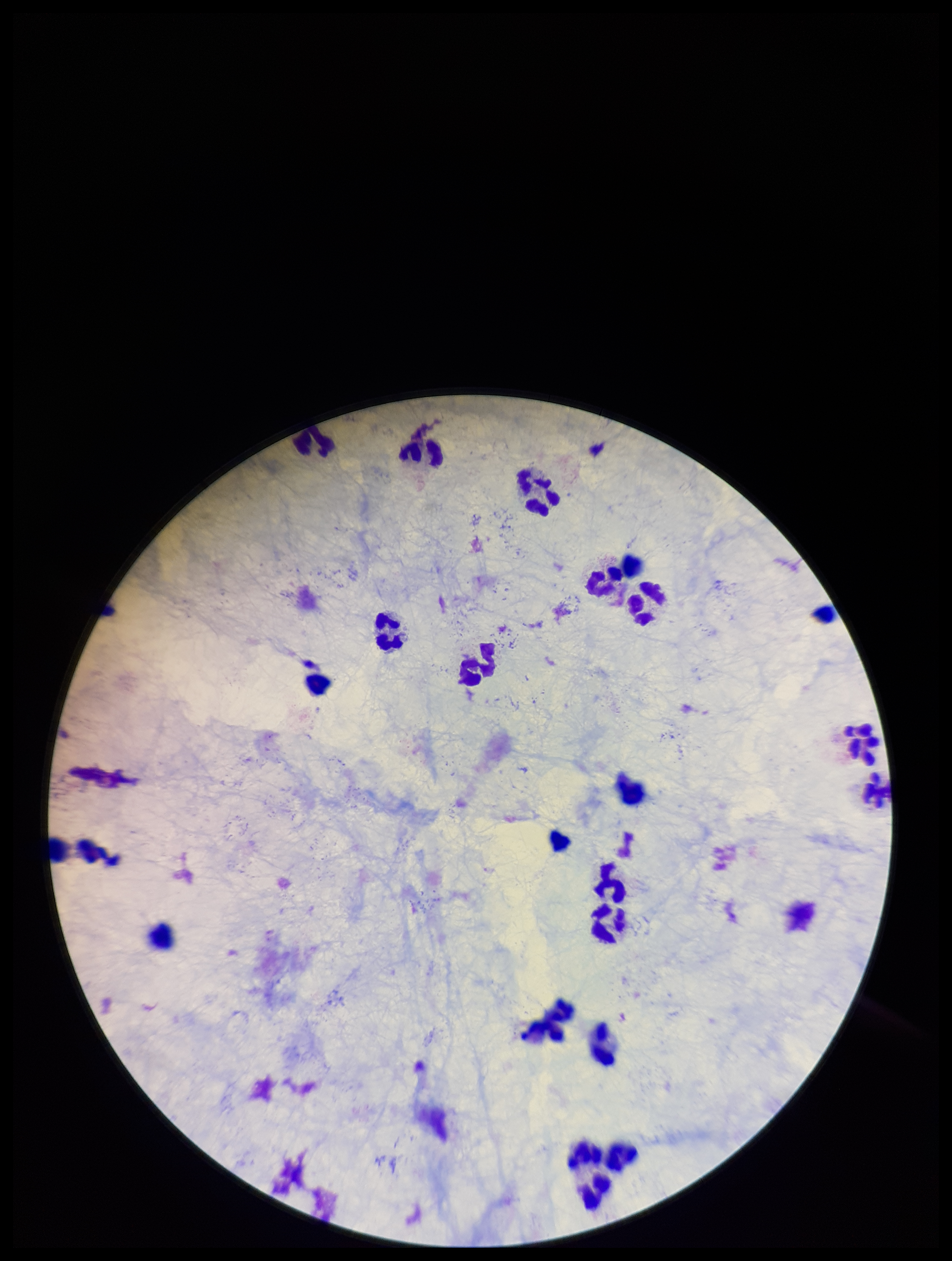
Summary:
  - Patient malaria status: negative
  - Plasmodium parasites: none identified
  - Image size: 952×1261 pixels
  - Leukocyte count: 20
  - Capture: smartphone photograph through the microscope eyepiece
  - Stain: Giemsa
  - Preparation: thick
  - Parasite count: 0
  - Field of view: one from this slide